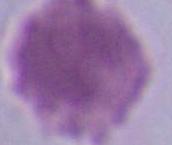
modality: micrograph
identification: erythrocyte
magnification: 1000x